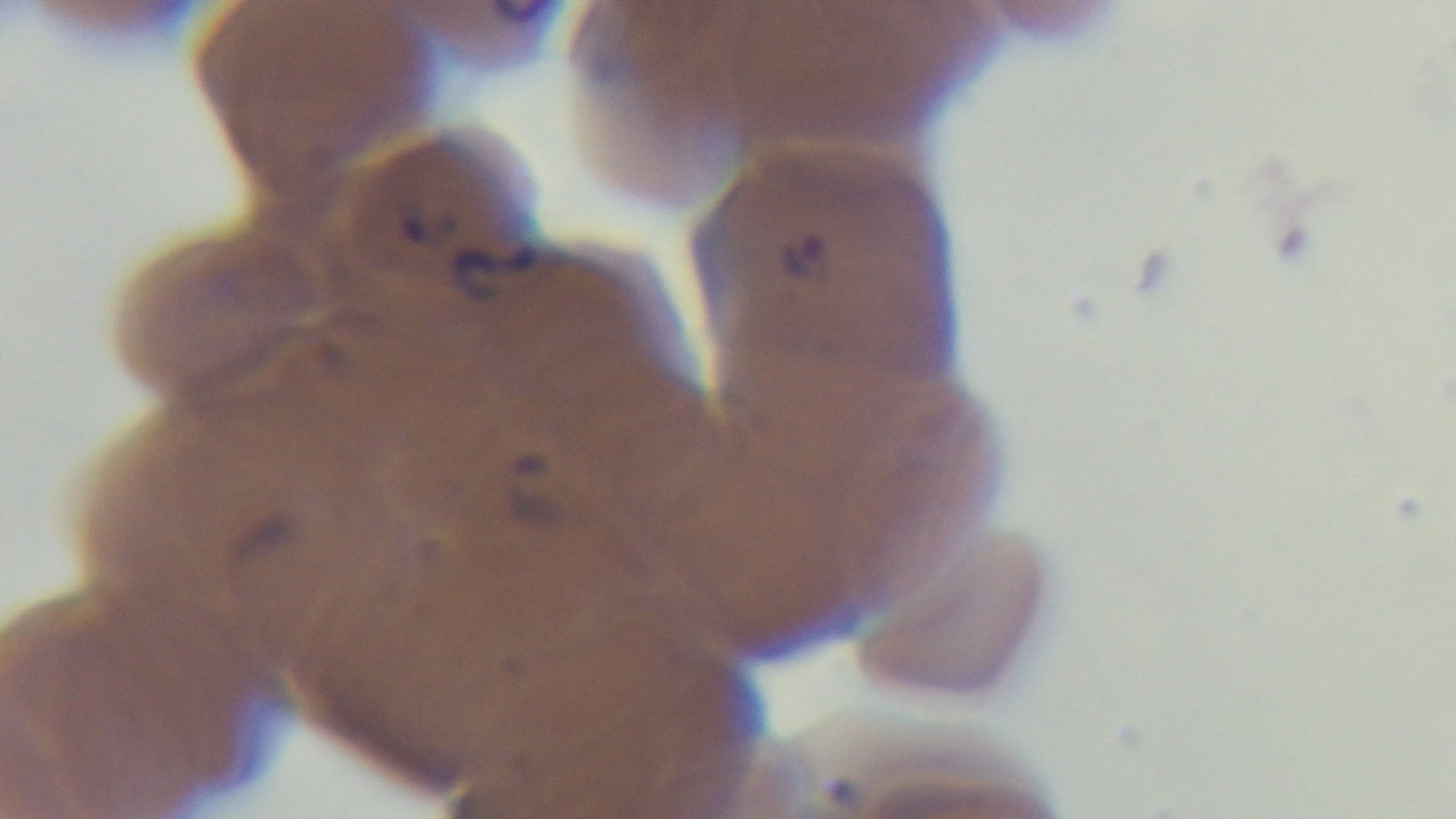
Summary:
  - Stain: Giemsa
  - Modality: light microscopy
  - Objective: 100x oil immersion
  - Capture: mounted 4K digital camera
  - Preparation: thin blood film
  - Field of view: single
  - Malaria status: positive